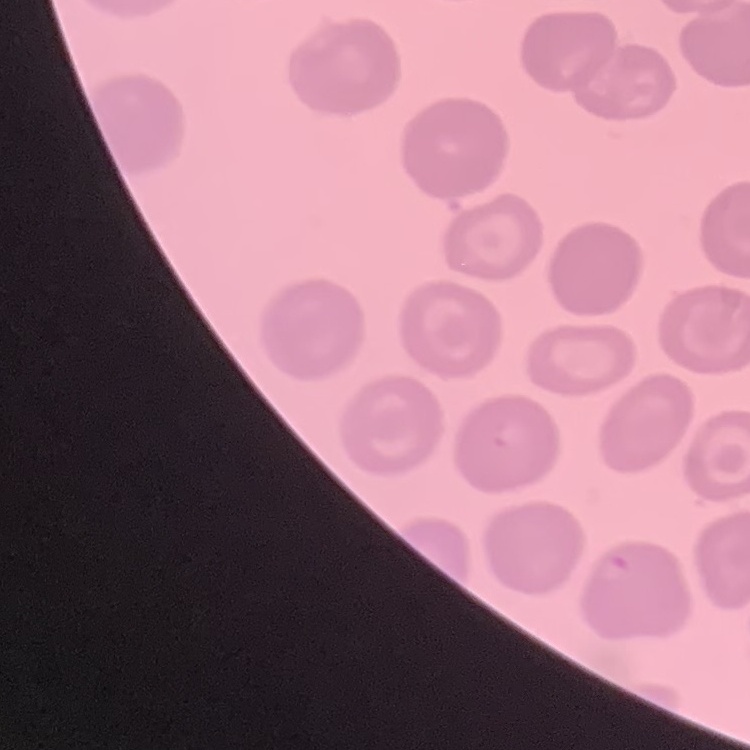

The red blood cells exhibit no rouleaux formation. Thin blood film. Field's or Giemsa stain. Square crop of a larger photomicrograph.